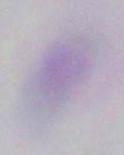

Summary:
  - Magnification: 1000x
  - Modality: micrograph
  - Identification: Toxoplasma gondii